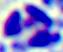
Summary:
  - Identification: leukocyte
  - Modality: micrograph
  - Magnification: 400x